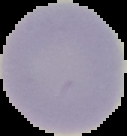

preparation: thin blood film
image_size: 127×136 pixels
result: negative for malaria parasites
image_type: cell region segmented out of the field of view; surrounding area masked to black